Locate every malaria parasite.
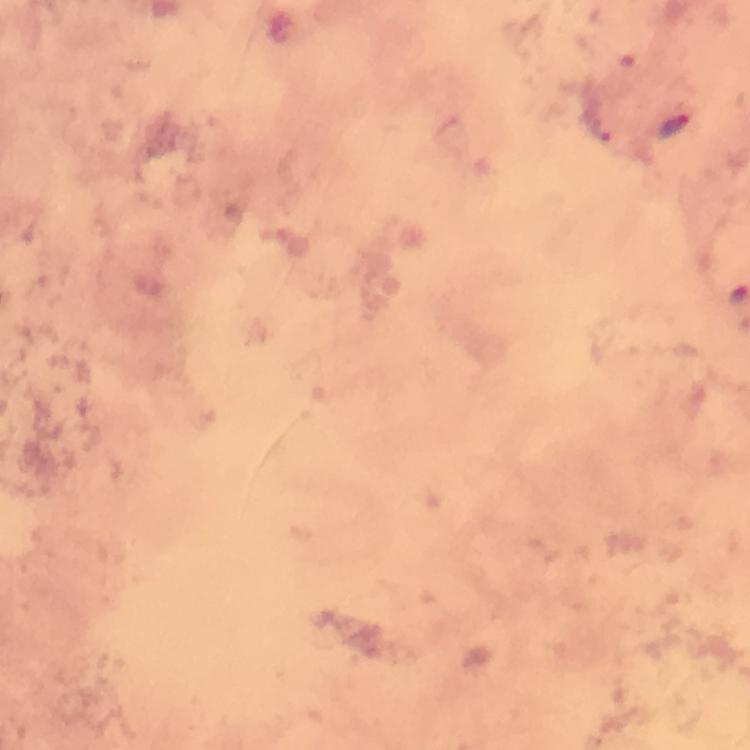
Approximate centers as {x, y} in pixels.
Malaria parasites: {675, 125}.

Summary:
  - Context: from a malaria diagnostic workup
  - Stain: Giemsa
  - Magnification: 100x
  - Cropped from: one field of view
  - Capture: smartphone mounted on the microscope
  - Immersion oil: applied
  - Preparation: thick smear
  - Image size: 750×750 pixels